Name the cell type shown.
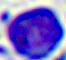
A leukocyte.

400x magnification. Micrograph.